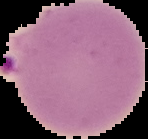
result: Plasmodium parasites identified
image_type: cell region segmented out of the field of view; surrounding area masked to black
image_size: 148×139 pixels
preparation: thin blood film